Identify the cell.
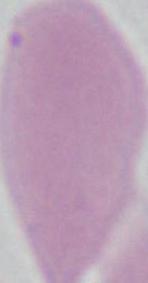
An erythrocyte.

magnification = 1000x
modality = micrograph